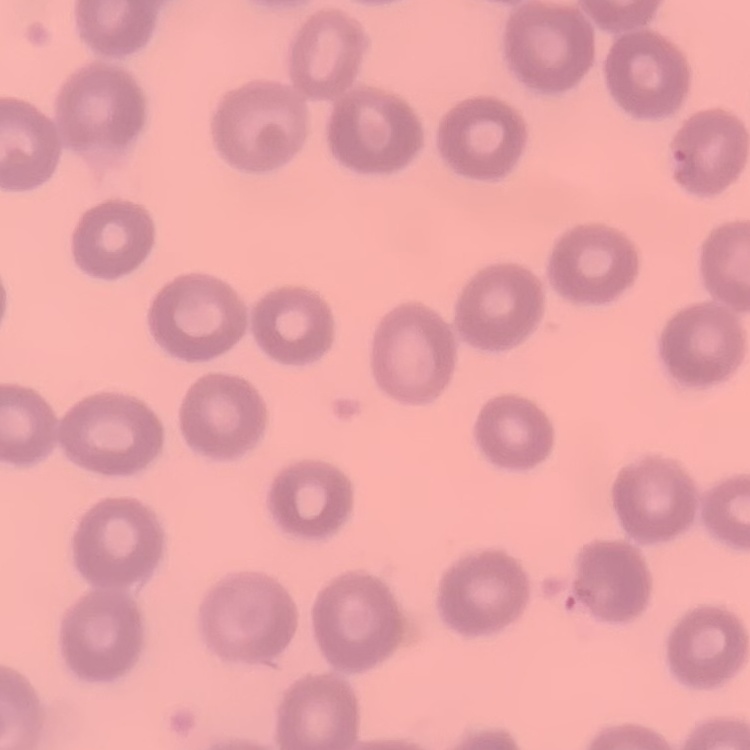
erythrocyte morphology = no rouleaux formation
stain = Field's or Giemsa
preparation = thin blood film
image type = square crop of a larger photomicrograph